Identify the blood parasite species.
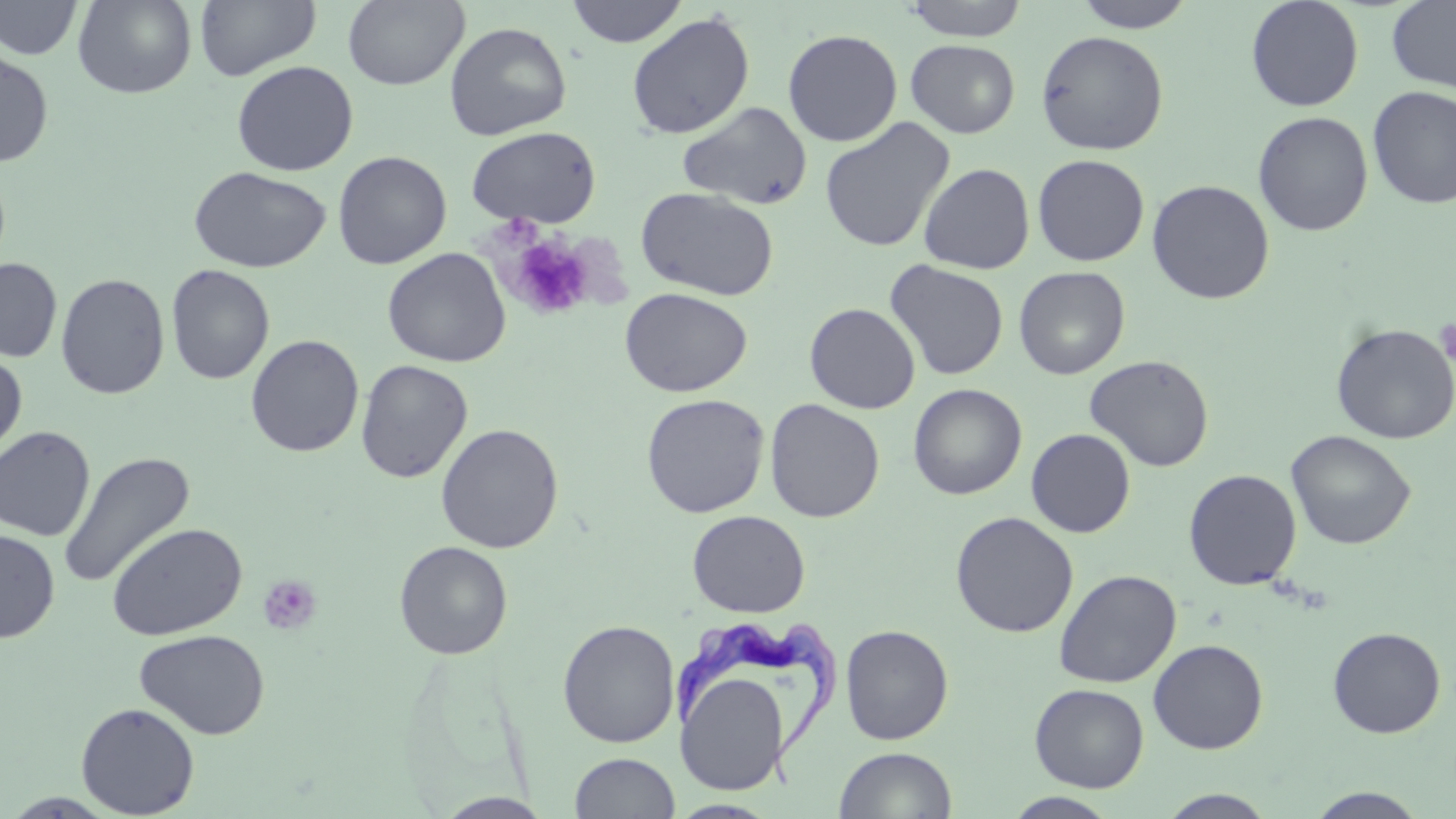

Trypanosoma brucei.

Summary:
  - Coordinate format: approximate bounding boxes as (x1, y1, x2, y2) in pixels
  - Trypanosoma brucei locations: (672, 617, 842, 792)
  - Uninfected red blood cell locations: (72, 0, 197, 98), (194, 0, 321, 81), (342, 0, 470, 90), (565, 0, 689, 47), (901, 0, 1030, 41), (1071, 0, 1196, 31), (1245, 0, 1364, 111), (1386, 0, 1456, 93), (0, 1, 83, 60), (626, 12, 755, 139), (445, 21, 571, 140), (782, 28, 903, 146), (1035, 30, 1169, 155), (905, 39, 1020, 138), (0, 48, 55, 167), (231, 60, 358, 176), (1367, 85, 1456, 209), (677, 101, 813, 210), (1252, 111, 1373, 236), (819, 118, 955, 253), (466, 126, 601, 228), (333, 150, 451, 269), (1032, 154, 1149, 266), (918, 162, 1035, 275), (188, 166, 331, 273), (1147, 179, 1275, 304), (635, 187, 779, 301), (382, 247, 511, 368), (1, 257, 63, 362), (885, 260, 1009, 380), (166, 264, 275, 385), (1014, 266, 1130, 379), (55, 273, 170, 399), (620, 287, 752, 397), (804, 302, 920, 414), (1330, 323, 1456, 444), (245, 334, 364, 457), (0, 348, 27, 460), (1084, 355, 1214, 472), (355, 360, 472, 483), (907, 383, 1027, 500), (641, 393, 769, 518), (764, 398, 885, 523), (435, 423, 564, 553), (0, 426, 95, 541), (1026, 428, 1135, 537), (1284, 430, 1416, 550), (57, 451, 195, 589), (1183, 469, 1302, 590), (687, 509, 810, 617), (950, 511, 1078, 638), (107, 522, 248, 641), (0, 528, 60, 643), (394, 540, 513, 659), (1054, 569, 1181, 688), (557, 620, 680, 747), (840, 624, 954, 745), (1327, 626, 1446, 738), (134, 628, 270, 740), (1148, 639, 1268, 754), (676, 668, 791, 795), (1030, 683, 1149, 792), (76, 702, 200, 817), (833, 746, 957, 819), (569, 752, 680, 818), (1305, 788, 1430, 819), (1157, 789, 1278, 818), (4, 792, 120, 817), (1003, 792, 1120, 818), (435, 793, 557, 818), (667, 799, 779, 818)
  - Platelet locations: (505, 235, 596, 321), (1435, 318, 1456, 373), (257, 574, 322, 636)
  - Modality: light microscopy
  - Preparation: thin blood smear
  - Image size: 1456×819 pixels
  - Magnification: 1000x
  - Field of view: single
  - Stain: May-Grünwald-Giemsa